Identify the cell.
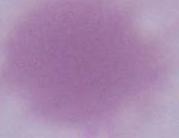
This is an erythrocyte.

modality = micrograph
magnification = 1000x